State the blood parasite species.
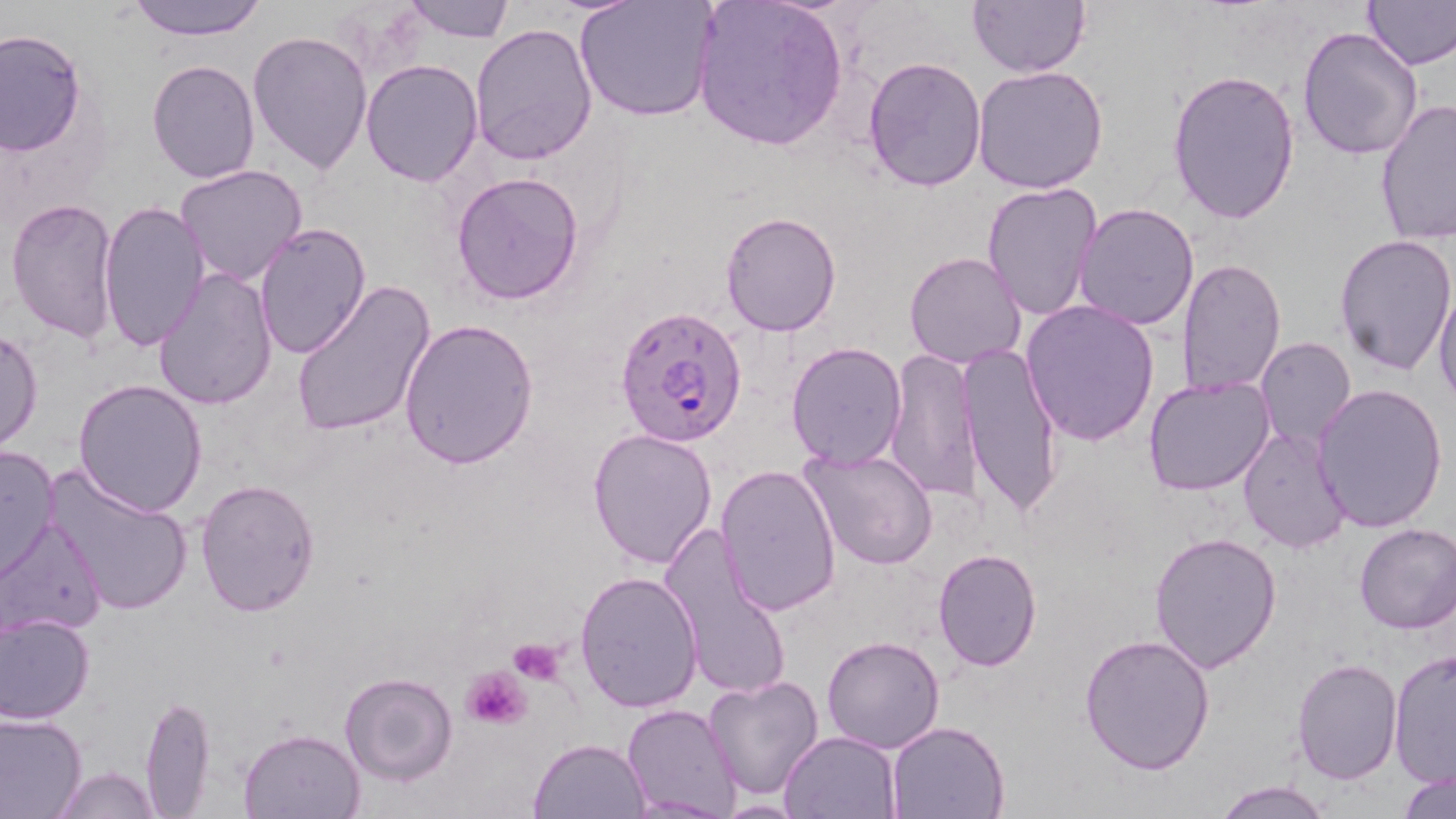
Plasmodium falciparum.

Summary:
  - Coordinate format: approximate bounding boxes as (x1,y1)-(x2,y2) corner pairs in pixels
  - Uninfected red blood cell locations: (124,0)-(267,41), (399,0)-(516,43), (576,0)-(719,123), (692,0)-(849,151), (967,0)-(1089,78), (1363,0)-(1456,69), (470,23)-(598,165), (1296,25)-(1424,162), (0,30)-(87,156), (247,30)-(373,174), (861,56)-(986,192), (147,59)-(260,184), (361,59)-(485,186), (973,64)-(1108,195), (1166,68)-(1300,226), (1375,99)-(1456,245), (175,163)-(308,288), (451,170)-(585,305), (981,182)-(1104,322), (5,197)-(121,345), (98,199)-(209,354), (1075,203)-(1201,331), (720,210)-(840,336), (254,222)-(373,360), (1333,234)-(1456,376), (904,250)-(1029,369), (1176,257)-(1287,396), (151,267)-(278,412), (291,279)-(436,439), (1433,285)-(1456,411), (1020,299)-(1160,446), (399,319)-(537,468), (0,324)-(43,454), (1256,338)-(1357,453), (785,340)-(908,469), (957,343)-(1064,518), (885,348)-(983,500), (1143,376)-(1275,496), (73,379)-(207,518), (1311,381)-(1447,532), (586,425)-(717,571), (1238,425)-(1354,555), (0,444)-(61,581), (801,449)-(938,571), (715,463)-(841,616), (40,465)-(196,620), (195,478)-(322,619), (2,516)-(108,638), (1352,522)-(1456,634), (659,523)-(793,703), (1148,530)-(1281,673), (933,549)-(1042,672), (575,569)-(704,713), (0,614)-(95,725), (1079,633)-(1215,775), (822,635)-(944,751), (1389,648)-(1456,787), (1293,659)-(1402,783), (338,671)-(458,786), (704,673)-(823,800), (140,694)-(219,818), (622,703)-(743,818), (0,711)-(86,818), (886,720)-(1011,818), (239,727)-(365,818), (780,729)-(900,819), (529,737)-(654,819), (52,765)-(162,819), (1399,770)-(1456,818), (1211,779)-(1334,818), (713,800)-(807,817)
  - Plasmodium falciparum-infected red blood cell locations: (616,309)-(751,451)
  - Platelet locations: (508,636)-(565,683), (461,664)-(532,731)
  - Modality: light microscopy
  - Stain: May-Grünwald-Giemsa
  - Preparation: thin blood smear
  - Image size: 1456×819 pixels
  - Magnification: 1000x
  - Field of view: single